Point out each leukocyte.
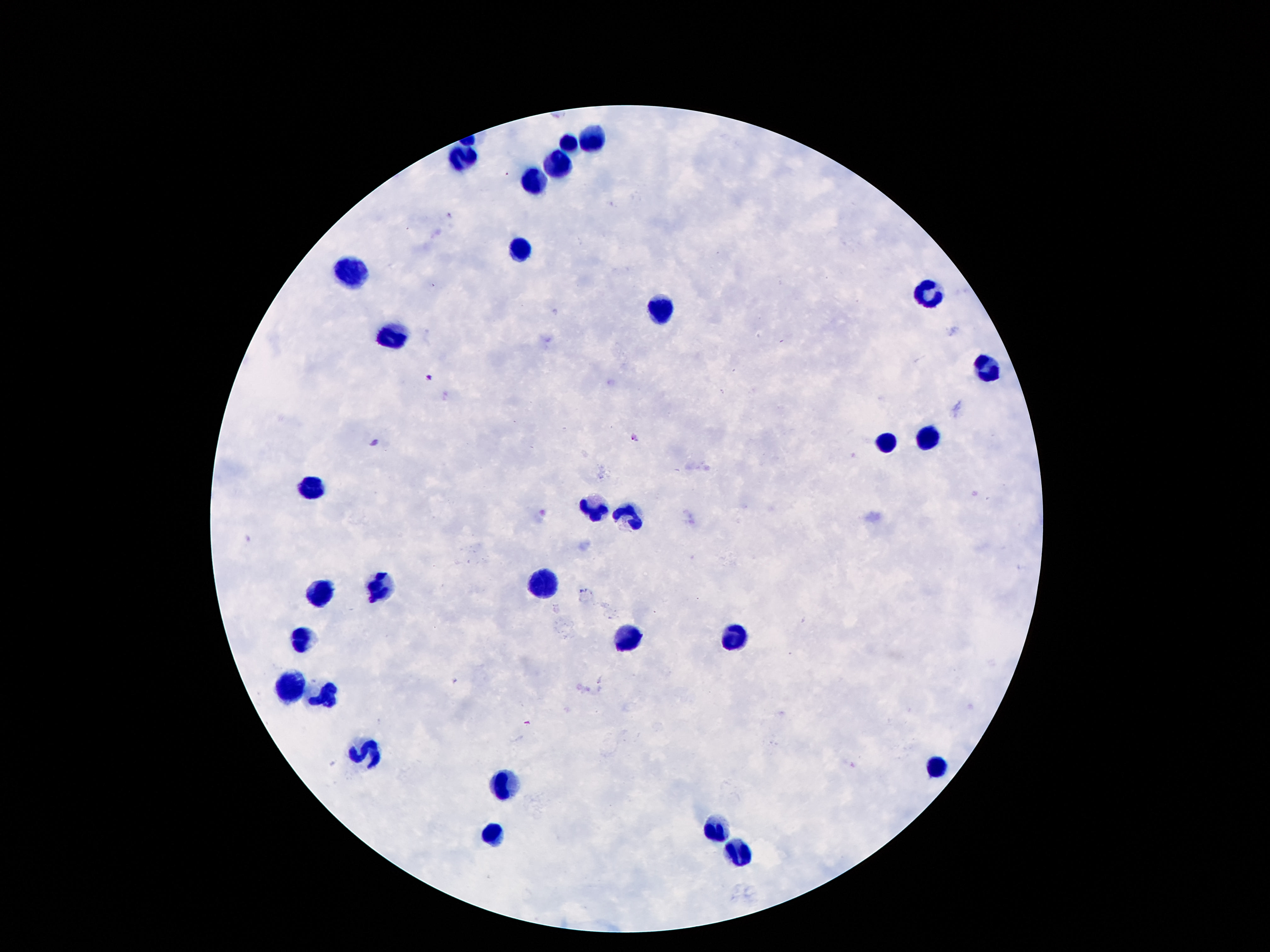

Approximate centers as {x, y} in pixels.
Leukocytes: {592, 136}, {567, 142}, {464, 158}, {557, 163}, {533, 181}, {517, 249}, {351, 274}, {929, 291}, {659, 308}, {394, 338}, {988, 372}, {927, 440}, {884, 441}, {312, 488}, {594, 510}, {626, 515}, {541, 584}, {380, 587}, {319, 592}, {732, 637}, {625, 640}, {299, 644}, {290, 685}, {322, 698}, {938, 766}, {508, 783}, {714, 828}, {491, 835}, {736, 853}.

Image is 1270×952 pixels. Smartphone photograph taken through the microscope eyepiece. Thick blood smear. Single field of view. 100x magnification. Giemsa stain. Patient malaria status: negative.